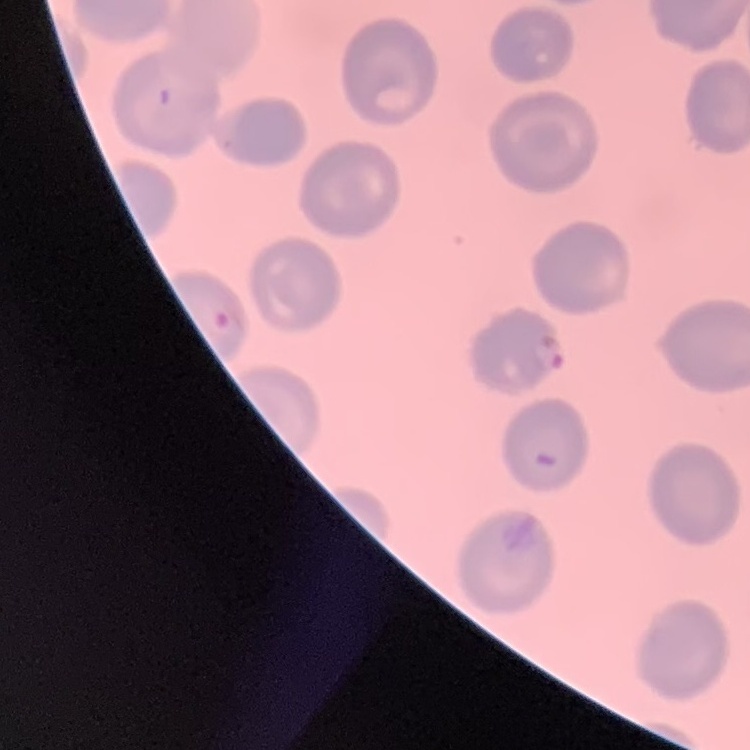
red blood cell morphology = no rouleaux formation
preparation = thin peripheral smear
image type = one tile cut from a larger photomicrograph
stain = Field's or Giemsa